Outline each blood parasite and name the species.
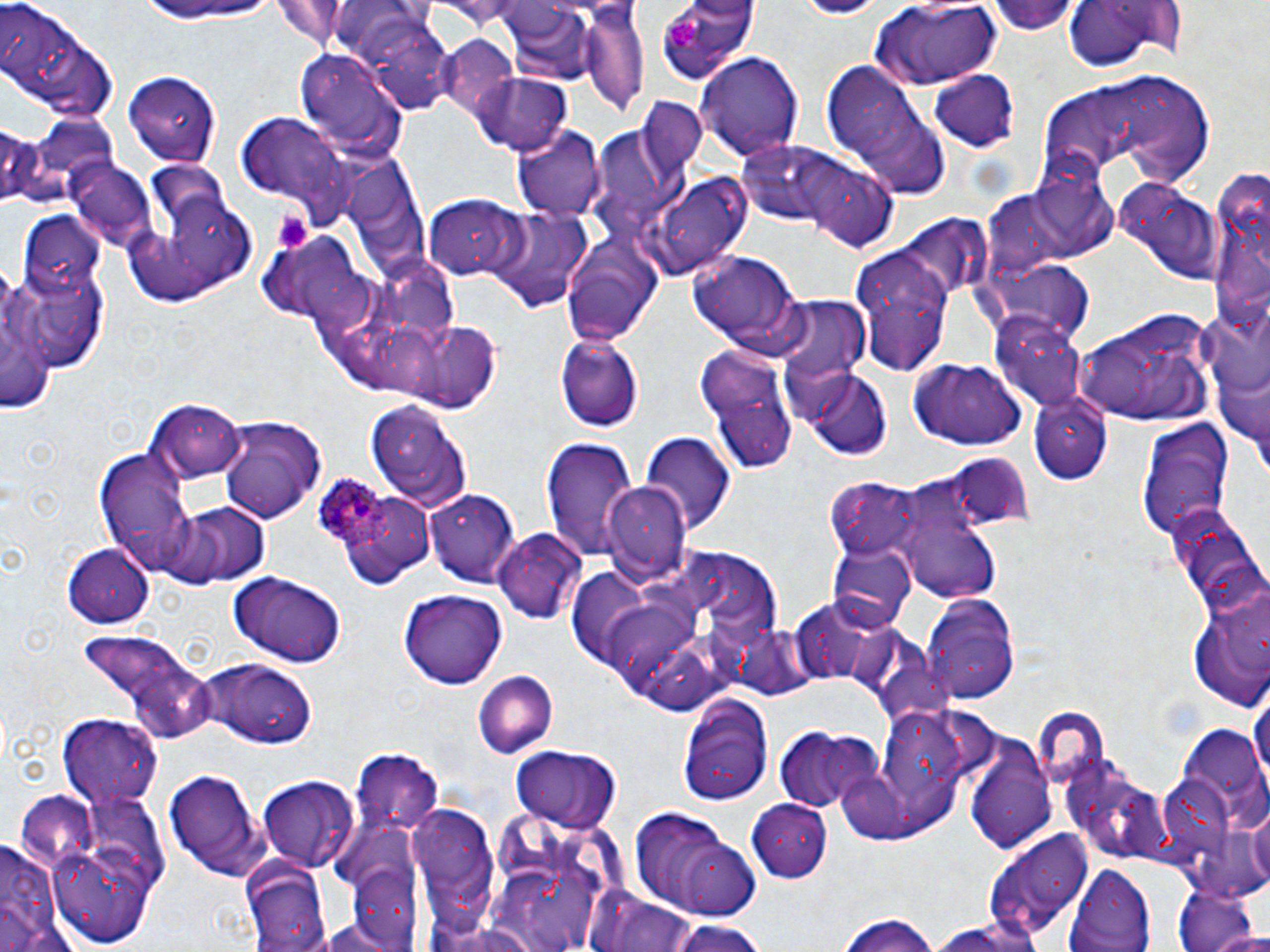
Approximate bounding boxes as (x1,y1)-(x2,y2) corner pairs in pixels.
Plasmodium ovale-infected red blood cells: (312,471)-(387,550).
No Plasmodium falciparum, Plasmodium malariae, Plasmodium vivax, Babesia divergens, or Trypanosoma brucei observed.

Summary:
  - Platelet locations: (666,15)-(703,50), (271,209)-(314,256)
  - Uninfected red blood cell locations: (0,0)-(115,119), (654,0)-(757,82), (131,1)-(283,29), (790,1)-(882,19), (993,1)-(1083,36), (584,2)-(648,120), (867,2)-(1005,85), (1060,2)-(1174,76), (498,4)-(596,86), (367,28)-(465,120), (438,34)-(518,118), (297,46)-(407,163), (698,52)-(803,161), (819,62)-(939,185), (121,68)-(221,166), (928,68)-(1023,151), (1095,73)-(1214,184), (469,74)-(572,156), (1044,87)-(1126,173), (643,93)-(708,172), (235,112)-(352,216), (0,125)-(47,206), (513,125)-(606,222), (596,125)-(697,210), (738,140)-(855,227), (800,157)-(899,251), (68,159)-(157,254), (1024,165)-(1118,263), (1204,167)-(1268,345), (124,174)-(259,308), (646,174)-(752,276), (1110,176)-(1222,285), (425,195)-(527,280), (486,205)-(590,311), (17,211)-(106,296), (897,215)-(991,308), (559,228)-(667,345), (850,244)-(952,374), (689,251)-(807,352), (299,264)-(378,331), (1,270)-(56,420), (11,276)-(106,375), (774,297)-(869,386), (1198,299)-(1268,450), (1077,309)-(1216,430), (991,311)-(1090,414), (395,319)-(503,412), (554,333)-(645,432), (696,347)-(796,472), (906,355)-(1027,451), (800,367)-(895,460), (1027,393)-(1116,484), (148,399)-(245,481), (364,399)-(471,513), (218,417)-(325,522), (1138,420)-(1233,545), (642,432)-(735,536), (542,436)-(638,559), (95,447)-(194,566), (959,460)-(1036,526), (826,479)-(929,565), (603,482)-(687,577), (425,486)-(521,584), (899,488)-(1006,605), (170,502)-(268,587), (1164,503)-(1266,614), (492,528)-(587,622), (60,542)-(154,624), (828,542)-(916,632), (226,572)-(347,668), (1184,576)-(1270,712), (399,588)-(508,690), (922,595)-(1021,705), (793,599)-(891,687), (604,600)-(698,692), (81,630)-(191,709), (193,661)-(318,749), (471,670)-(557,757), (131,671)-(213,742), (1250,684)-(1270,801), (678,694)-(771,805), (1031,707)-(1111,788), (883,708)-(967,801), (57,715)-(162,810), (776,728)-(882,815), (349,742)-(444,830), (512,748)-(616,831), (964,749)-(1058,853), (164,766)-(267,876), (1157,770)-(1237,864), (257,776)-(359,869), (14,791)-(102,875), (748,798)-(835,882), (408,804)-(500,925), (628,808)-(757,918), (985,831)-(1092,943), (1,836)-(67,952), (53,854)-(131,941), (239,858)-(333,951), (348,860)-(427,947), (1063,863)-(1156,952), (524,865)-(596,950), (1170,882)-(1262,952), (598,897)-(698,952), (833,912)-(945,952), (929,917)-(1049,952), (667,921)-(772,952)
  - Slide-level diagnosis: Plasmodium ovale
  - Magnification: 1000x
  - Stain: May-Grünwald-Giemsa
  - Image size: 1270×952 pixels
  - Modality: light microscopy
  - Preparation: thin blood film
  - Field of view: one of a larger specimen